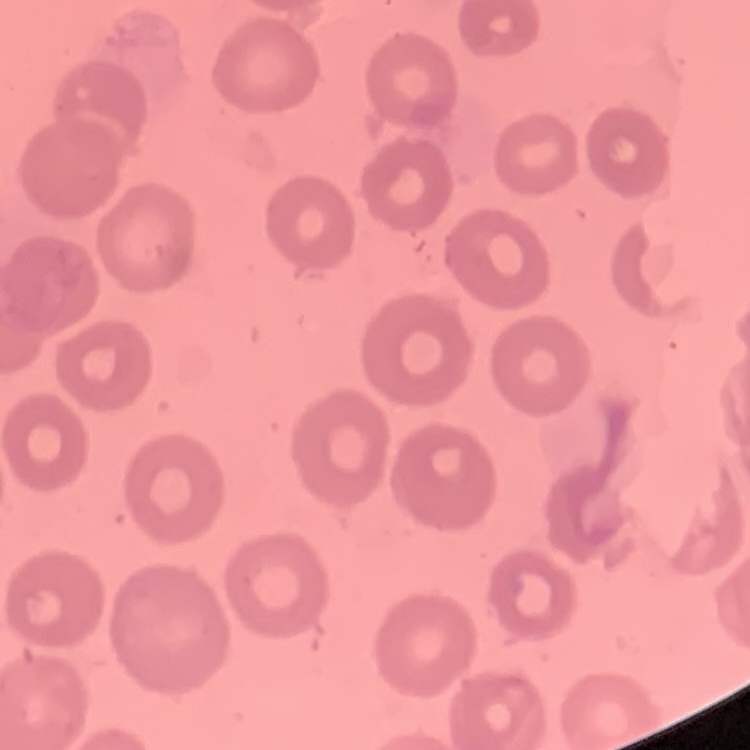
erythrocyte morphology = no rouleaux formation
image type = square crop of a larger photomicrograph
stain = Field's or Giemsa
preparation = thin peripheral smear